Name the parasite shown.
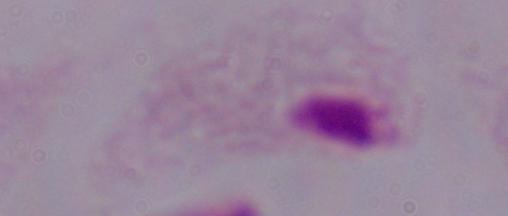
This is a trichomonad.

modality = micrograph
magnification = 1000x